Give the position of every Plasmodium parasite visible.
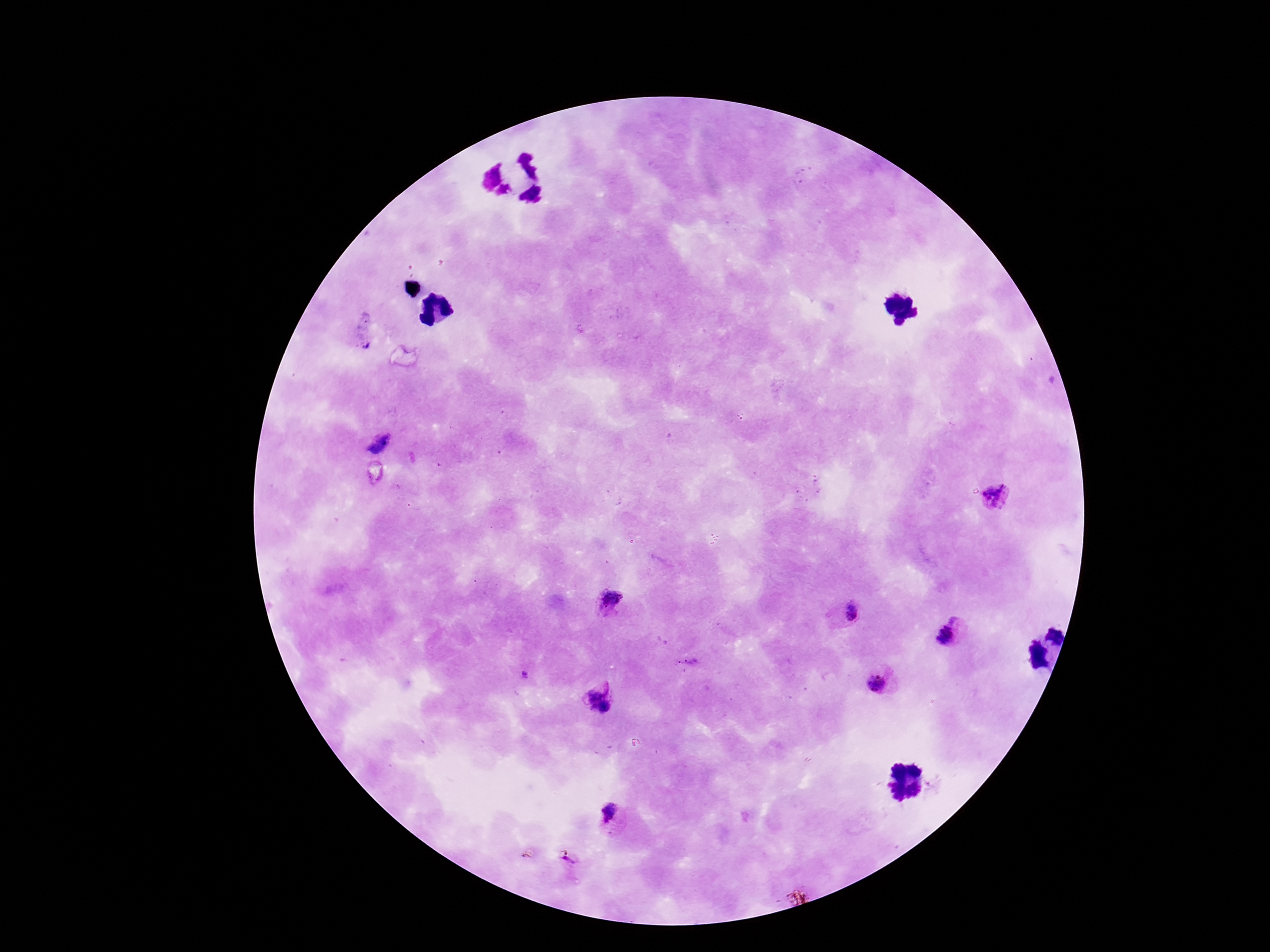
Approximate centers as {x, y} in pixels.
Plasmodium parasites: {995, 496}, {608, 602}, {852, 613}, {947, 635}, {525, 674}, {876, 683}, {592, 692}, {606, 707}, {592, 708}, {610, 815}, {569, 860}.

Summary:
  - Magnification: 100x
  - Preparation: thick peripheral-blood smear
  - Stain: Giemsa
  - Image size: 1270×952 pixels
  - Capture: smartphone camera through the microscope eyepiece
  - Field of view: single
  - Patient malaria status: infected